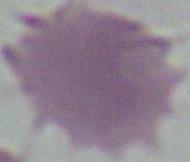
{
  "identification": "red blood cell",
  "magnification": "1000x",
  "modality": "micrograph"
}